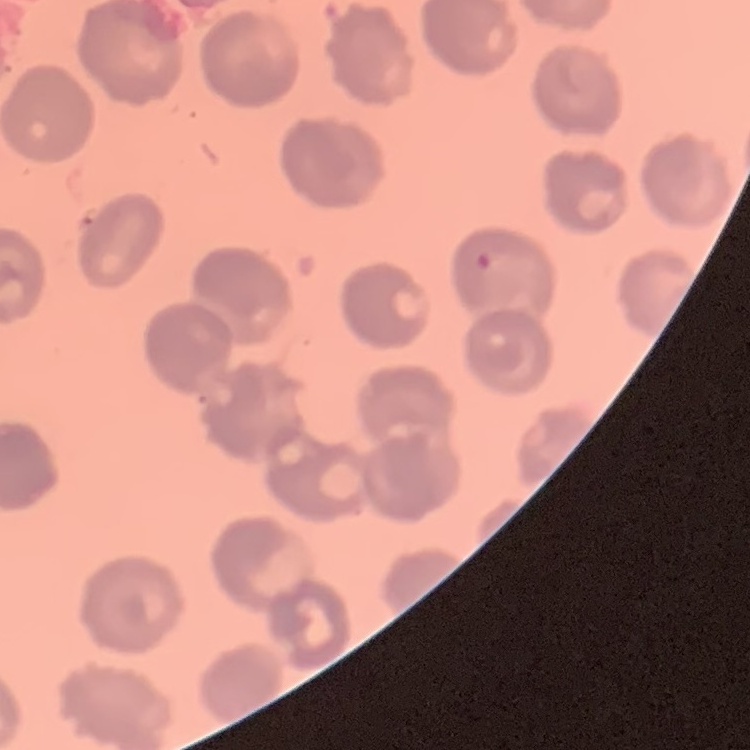

Summary:
  - Erythrocyte morphology: no rouleaux formation
  - Stain: Field's or Giemsa
  - Image type: square crop of a larger photomicrograph
  - Preparation: thin peripheral smear